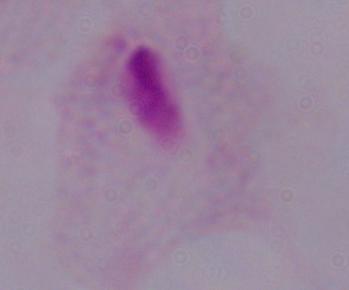

Captured at 1000x magnification. Micrograph. A trichomonad is seen.